Locate every leukocyte (white blood cell).
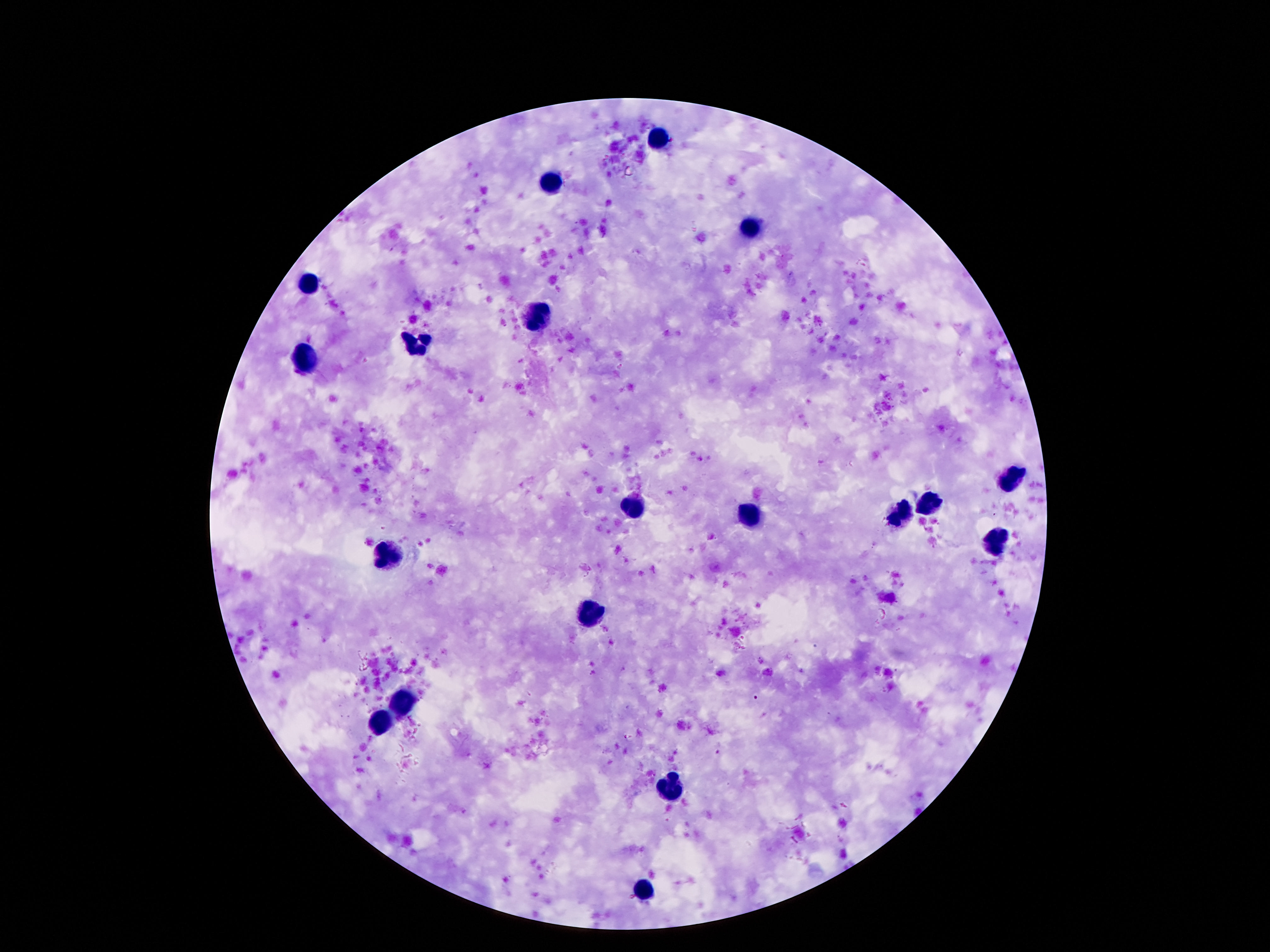

Approximate centers as [x, y] in pixels.
Leukocytes: [659, 139], [552, 185], [751, 230], [307, 286], [537, 317], [414, 344], [304, 361], [1014, 477], [928, 504], [630, 506], [749, 515], [898, 515], [999, 540], [390, 554], [590, 611], [405, 701], [378, 722], [668, 788], [642, 890].

Summary:
  - Image size: 1270×952 pixels
  - Preparation: thick blood smear
  - Patient malaria status: negative
  - Capture: smartphone camera through the microscope eyepiece
  - Magnification: 100x
  - Stain: Giemsa
  - Field of view: one from this slide